Identify the blood parasite species.
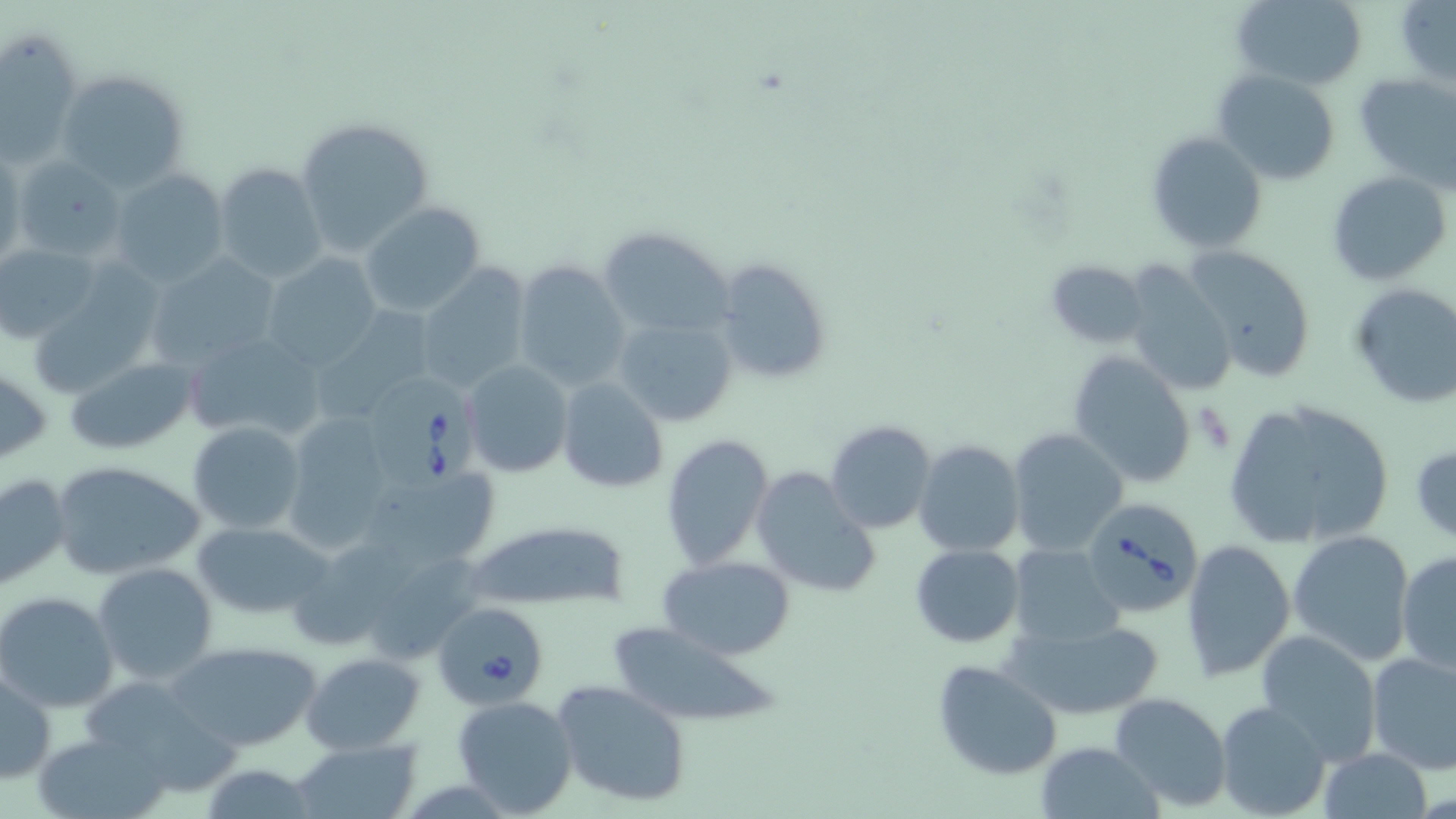
Babesia divergens.

Approximate bounding boxes as (x1, y1, x2, y2) in pixels. Uninfected red blood cell locations: (1231, 0, 1368, 90), (1396, 2, 1456, 88), (2, 29, 83, 164), (57, 68, 188, 191), (1214, 70, 1341, 185), (1354, 73, 1455, 189), (295, 117, 435, 257), (1146, 130, 1268, 253), (0, 147, 23, 271), (10, 157, 125, 264), (213, 162, 326, 282), (110, 168, 230, 289), (1327, 171, 1452, 286), (361, 203, 486, 316), (597, 224, 737, 339), (0, 243, 102, 345), (1183, 243, 1317, 383), (145, 254, 279, 369), (260, 256, 379, 370), (713, 256, 835, 385), (1044, 258, 1149, 348), (1119, 259, 1237, 397), (511, 261, 629, 392), (413, 265, 531, 394), (25, 267, 168, 403), (1348, 282, 1456, 410), (314, 304, 434, 421), (613, 317, 738, 428), (180, 329, 326, 444), (1068, 352, 1197, 489), (65, 357, 199, 455), (463, 360, 572, 478), (0, 365, 50, 468), (556, 377, 669, 494), (1221, 398, 1395, 551), (281, 411, 398, 549), (826, 419, 937, 534), (189, 422, 306, 533), (1007, 427, 1128, 555), (662, 434, 776, 571), (914, 440, 1024, 556), (1411, 441, 1456, 545), (50, 460, 207, 580), (356, 461, 505, 574), (751, 467, 881, 598), (0, 472, 72, 593), (462, 517, 635, 611), (191, 520, 335, 622), (1288, 529, 1416, 667), (284, 535, 429, 648), (1180, 537, 1297, 682), (1007, 543, 1123, 648), (910, 544, 1025, 647), (1395, 550, 1456, 674), (657, 554, 797, 660), (366, 558, 491, 668), (92, 561, 218, 684), (0, 591, 119, 711), (1007, 618, 1165, 719), (604, 622, 787, 728), (1255, 631, 1382, 765), (165, 641, 322, 750), (1366, 650, 1456, 774), (300, 652, 426, 755), (933, 660, 1061, 779), (1, 667, 59, 784), (551, 679, 695, 808), (1110, 691, 1233, 810), (451, 694, 579, 817), (1215, 701, 1331, 819), (34, 730, 171, 819), (290, 739, 421, 818), (1035, 740, 1163, 819), (1318, 748, 1433, 818). Babesia divergens-infected red blood cell locations: (375, 378, 480, 492), (1087, 501, 1202, 615), (434, 599, 549, 709). Image is 1456×819 pixels. Single field of view. Thin blood film. Light microscopy. May-Grünwald-Giemsa stain. Captured at 1000x magnification.